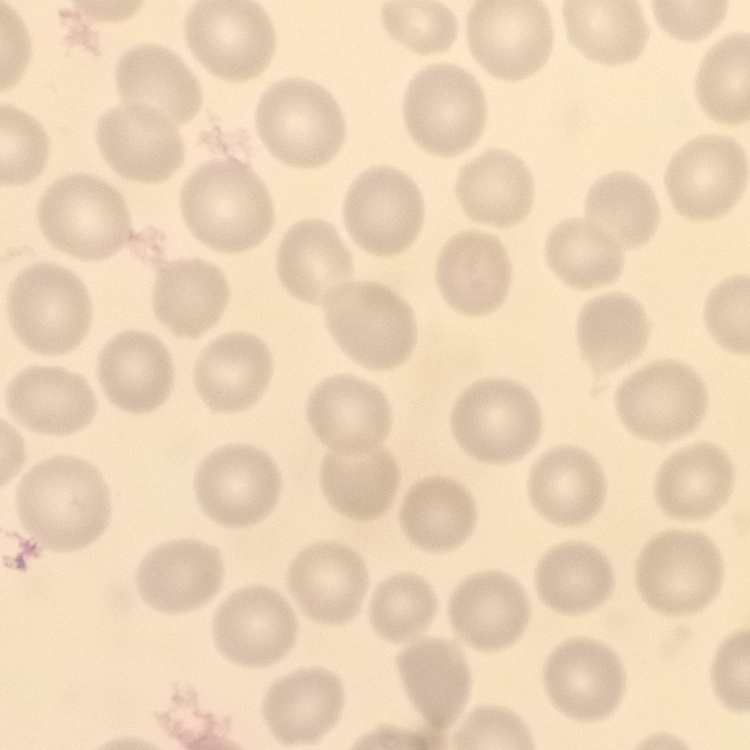

Summary:
  - Erythrocyte morphology: no rouleaux formation
  - Preparation: thin blood smear
  - Image type: one tile cut from a larger photomicrograph
  - Stain: Field's or Giemsa